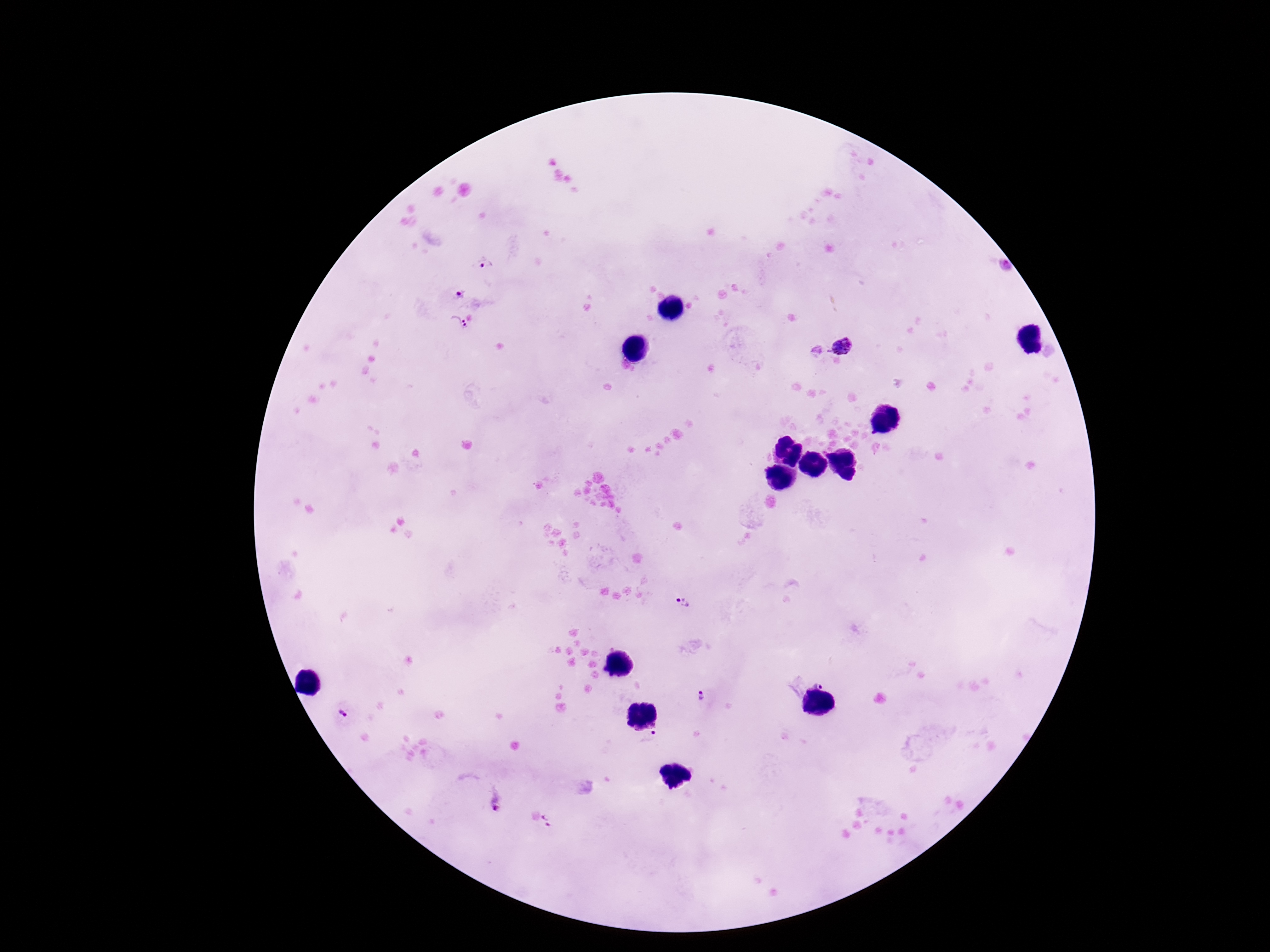
patient malaria status = infected
Plasmodium parasite locations = approximate centers as (x, y) in pixels: (483, 261), (459, 296), (458, 323), (843, 347), (683, 602), (819, 683), (702, 697), (342, 715), (649, 737), (495, 802), (546, 821)
image size = 1270×952 pixels
magnification = 100x
field of view = single
stain = Giemsa
capture = smartphone camera through the microscope eyepiece
preparation = thick peripheral-blood smear